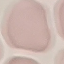
Summary:
  - Result: no malaria parasites detected
  - Capture: smartphone camera at the microscope eyepiece
  - Preparation: thin smear
  - Image type: automatically extracted cell patch, resized to 64 × 64 pixels
  - Stain: Giemsa